Assess for Plasmodium parasites.
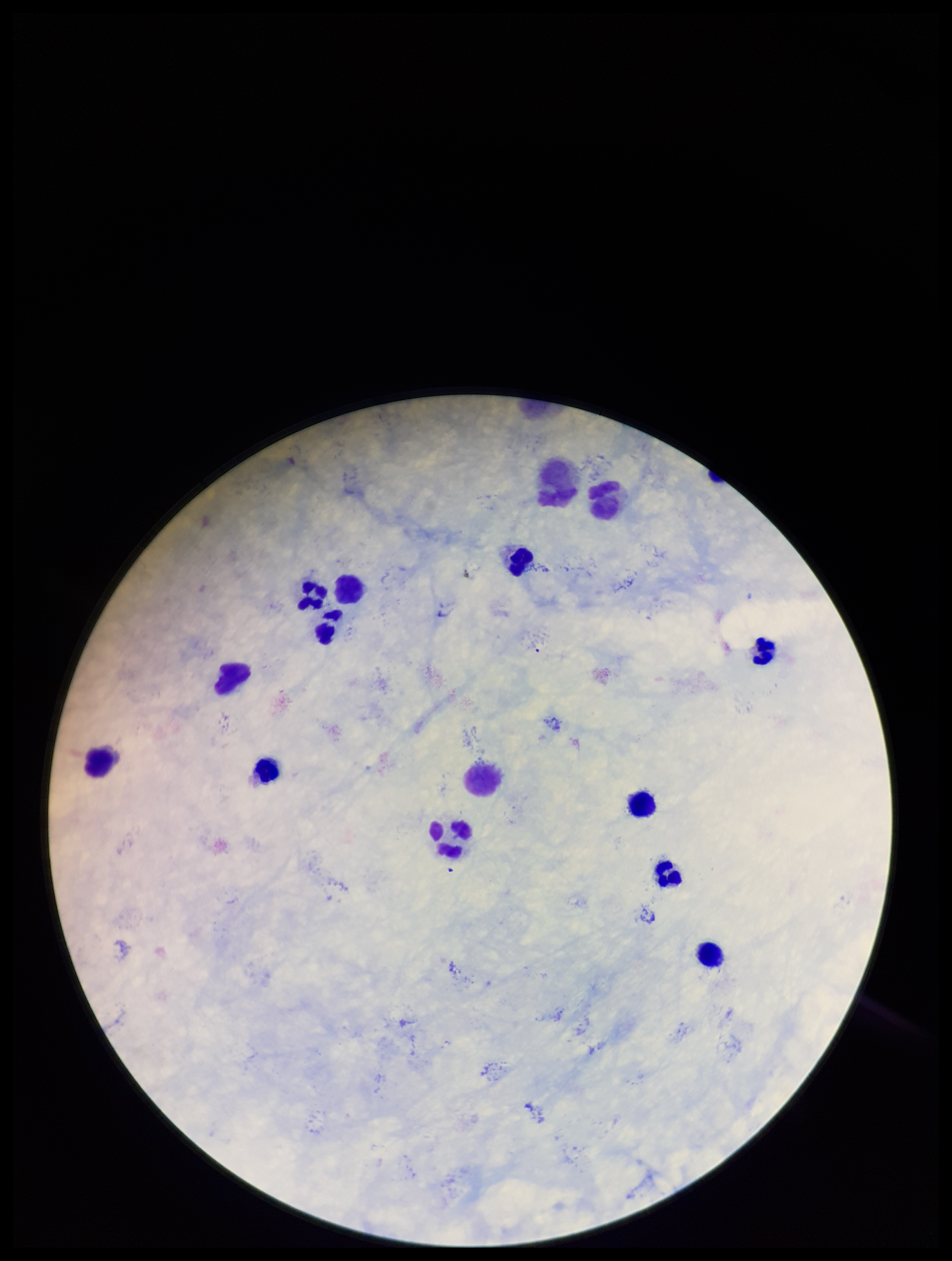
None detected.

Image is 952×1261 pixels. Giemsa stain. Leukocyte count: 12. Preparation: thick smear. Parasite count: 0. Patient malaria status: negative. Photographed through the microscope eyepiece with a smartphone camera. One field from this slide.